Classify this cell by malaria status.
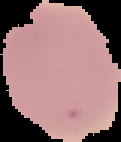
It is uninfected.

Summary:
  - Image type: segmented cell region with the area outside set to black
  - Preparation: thin blood smear
  - Image size: 121×142 pixels